Locate and identify every blood parasite.
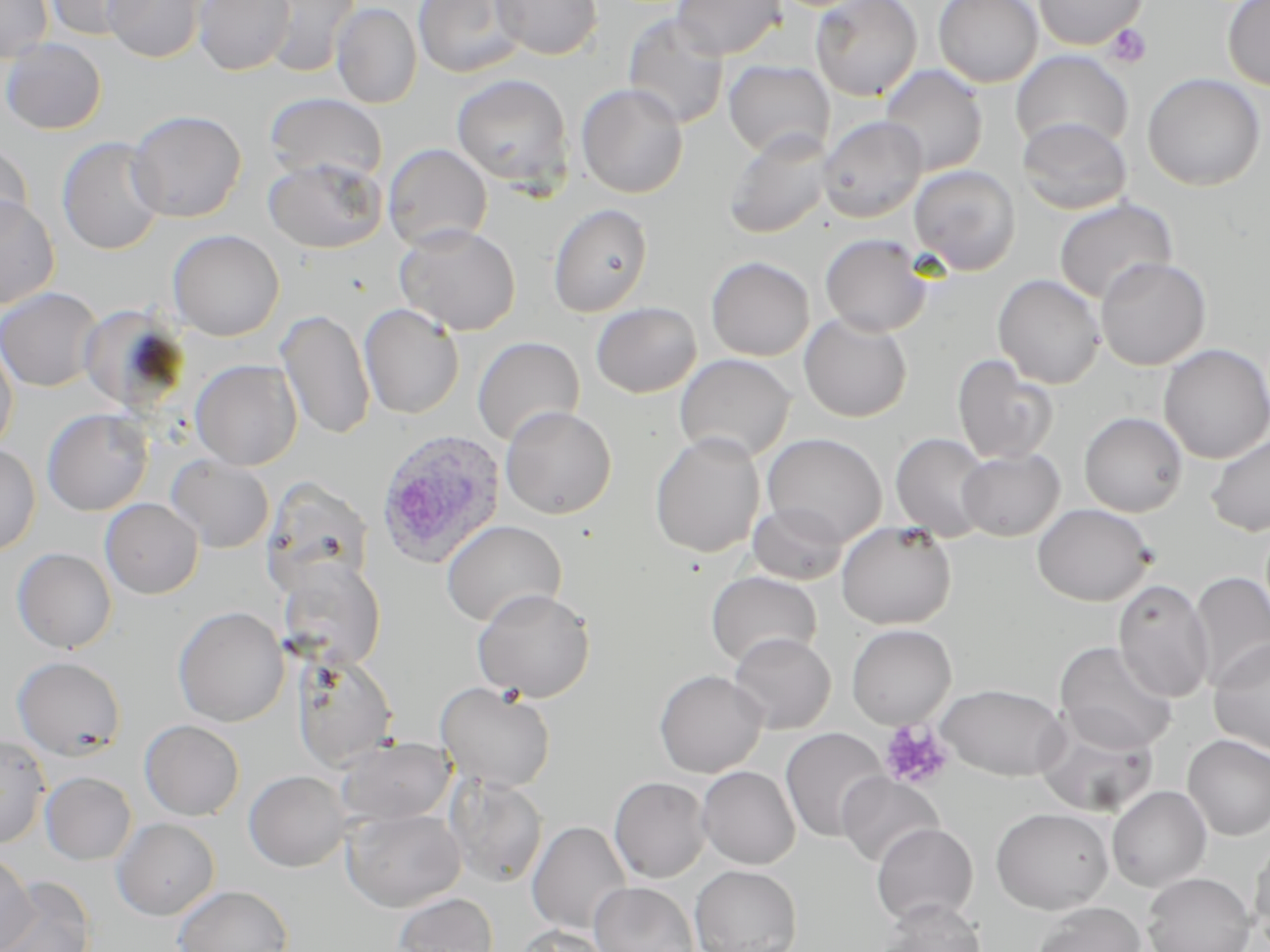

Approximate bounding boxes as (x1,y1)-(x2,y2) corner pairs in pixels.
Plasmodium ovale-infected red blood cells: (375,429)-(507,570).
No Plasmodium falciparum, Plasmodium malariae, Plasmodium vivax, Babesia divergens, or Trypanosoma brucei observed.

Platelet locations: (1105,25)-(1151,67), (879,721)-(953,791). Uninfected red blood cell locations: (0,0)-(53,64), (45,0)-(156,40), (103,0)-(207,63), (193,0)-(295,76), (262,0)-(360,77), (413,0)-(527,78), (491,0)-(603,60), (671,0)-(785,60), (809,0)-(922,101), (934,0)-(1043,88), (1033,0)-(1146,50), (1222,0)-(1270,91), (331,2)-(422,109), (623,13)-(730,130), (1,38)-(107,135), (1011,51)-(1134,154), (723,60)-(834,159), (880,65)-(987,176), (451,73)-(573,190), (1142,73)-(1266,191), (576,83)-(688,198), (265,93)-(387,183), (126,109)-(247,223), (818,115)-(928,222), (1017,116)-(1132,215), (723,128)-(834,239), (57,137)-(165,255), (0,143)-(33,239), (384,144)-(492,251), (264,158)-(388,254), (909,164)-(1021,275), (0,194)-(59,310), (1054,198)-(1177,305), (547,203)-(653,317), (394,223)-(521,335), (168,229)-(284,341), (820,234)-(933,337), (695,256)-(805,462), (706,256)-(814,361), (1096,257)-(1211,370), (993,274)-(1105,389), (0,287)-(103,392), (591,301)-(702,398), (78,302)-(190,414), (359,304)-(464,419), (277,308)-(377,441), (799,313)-(912,421), (472,337)-(584,446), (0,339)-(18,458), (1158,344)-(1270,463), (674,354)-(795,462), (952,354)-(1060,463), (191,359)-(302,470), (500,406)-(616,519), (42,408)-(153,516), (1078,411)-(1188,517), (650,431)-(765,558), (761,433)-(887,546), (890,433)-(993,541), (1206,434)-(1270,536), (0,442)-(40,556), (957,448)-(1064,541), (167,456)-(274,553), (262,478)-(372,596), (100,498)-(203,599), (747,502)-(849,585), (1033,503)-(1155,605), (441,520)-(566,627), (836,521)-(956,629), (12,547)-(117,653), (277,560)-(386,670), (706,571)-(822,668), (1190,571)-(1270,691), (1113,578)-(1215,702), (472,588)-(596,702), (173,606)-(289,727), (846,624)-(956,729), (728,632)-(835,733), (1209,638)-(1270,757), (1054,640)-(1179,754), (292,654)-(399,772), (12,655)-(127,760), (654,670)-(767,777), (435,682)-(557,792), (936,683)-(1069,781), (1036,715)-(1159,818), (139,719)-(245,821), (780,727)-(889,842), (0,734)-(50,849), (1182,734)-(1270,840), (337,737)-(454,825), (696,766)-(801,869), (244,770)-(351,872), (40,771)-(136,865), (836,772)-(943,867), (447,776)-(549,888), (609,776)-(711,883), (1107,785)-(1212,892), (991,807)-(1114,914), (342,809)-(466,911), (111,818)-(219,920), (527,821)-(632,935), (871,822)-(978,925), (1249,836)-(1270,949), (0,851)-(36,952), (690,865)-(801,952), (1142,872)-(1256,952), (0,876)-(95,952), (589,882)-(699,952), (173,885)-(293,952), (393,893)-(498,952), (876,899)-(986,952), (1033,902)-(1146,952), (516,925)-(613,952). Slide-level diagnosis: Plasmodium ovale. Image is 1270×952 pixels. Thin blood film. May-Grünwald-Giemsa-stained preparation. One field of a larger specimen. Optical microscopy. Captured at 1000x magnification.